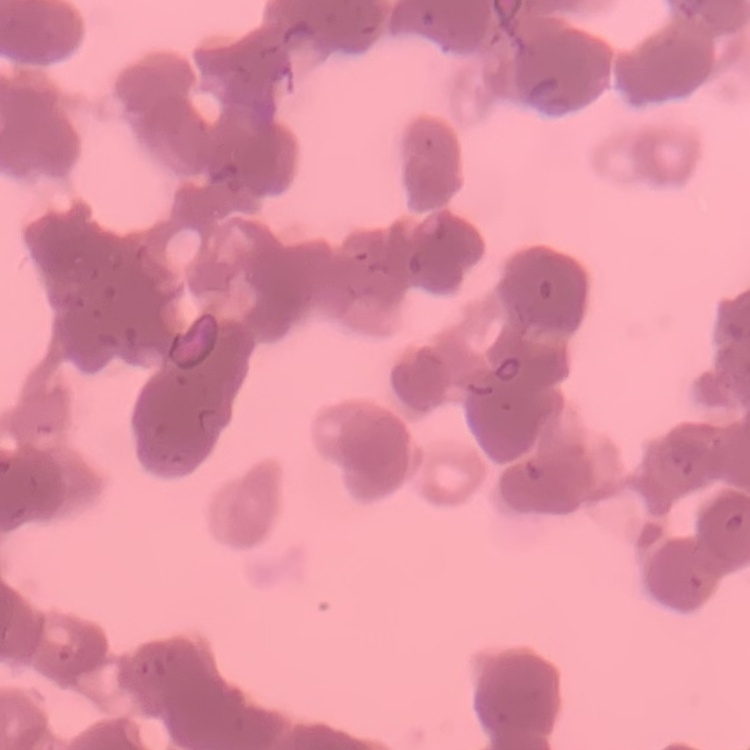 The red blood cells exhibit rouleaux formation. One tile cut from a larger photomicrograph. Field's or Giemsa stain. Thin peripheral smear.